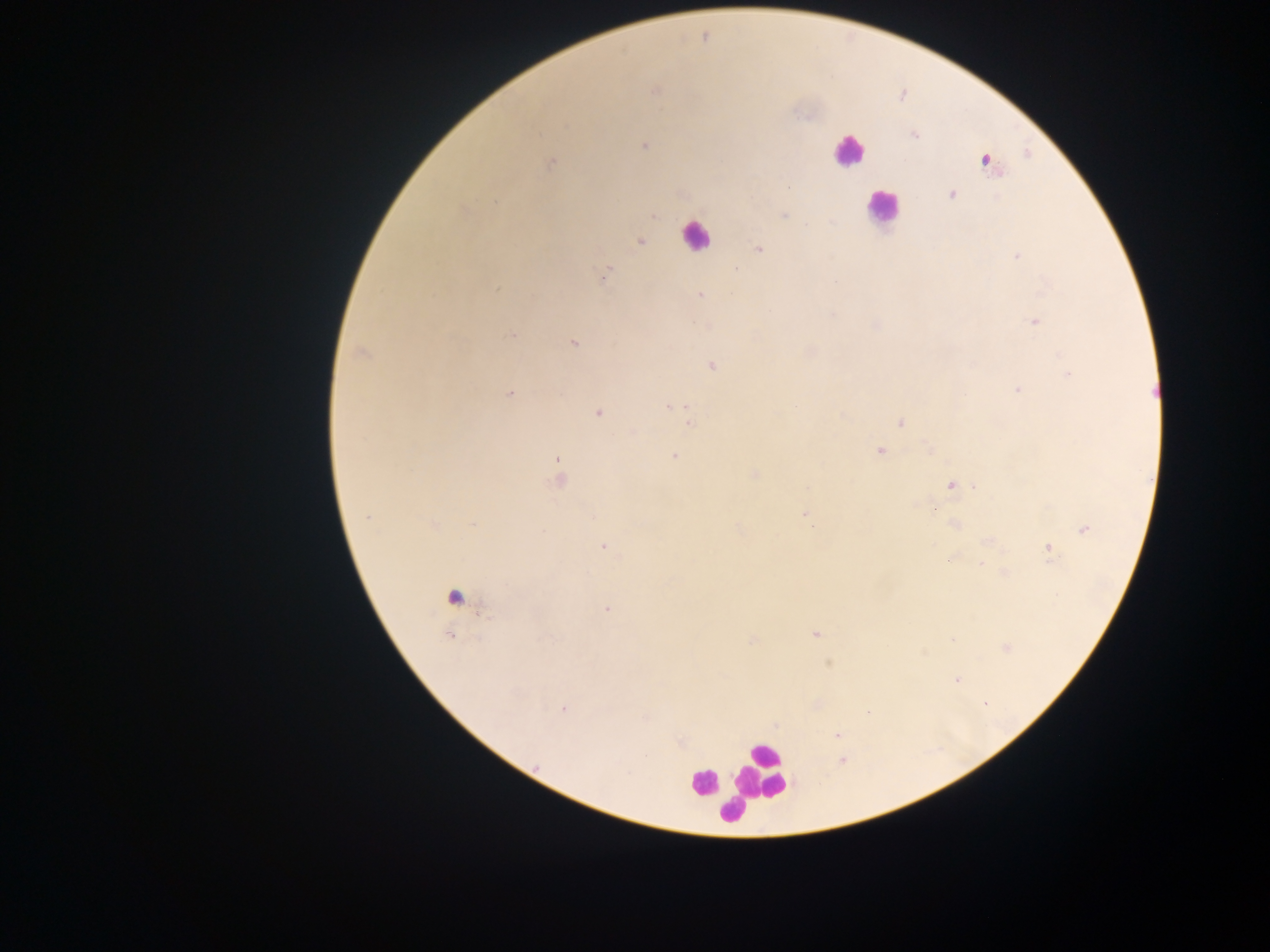
Approximate centers as (x, y) in pixels. Malaria parasite locations: (655, 90), (914, 135), (644, 145), (986, 161), (551, 163), (951, 194), (653, 215), (784, 215), (640, 242), (758, 249), (1017, 256), (737, 269), (605, 274), (497, 289), (700, 295), (1035, 322), (513, 335), (574, 342), (362, 352), (712, 365), (1068, 373), (1018, 389), (509, 394), (676, 405), (599, 412), (683, 412), (843, 416), (900, 423), (690, 424), (880, 451), (675, 456), (557, 460), (754, 475), (559, 478), (951, 485), (935, 508), (804, 516), (366, 517), (472, 524), (433, 525), (954, 525), (1084, 529), (991, 542), (604, 547), (1049, 548), (953, 559), (982, 565), (1004, 573), (606, 609), (815, 634), (449, 635), (952, 640), (751, 641), (1006, 648), (956, 680), (984, 704), (563, 708), (646, 718), (837, 735), (843, 761). Leukocyte locations: (848, 152), (881, 208), (695, 236), (452, 596), (763, 770), (702, 784), (734, 810). Single field of view. Image is 1270×952 pixels. Thick blood smear. Mobile-phone photograph taken through the microscope. Collected in Ghana.